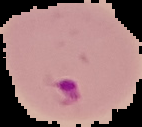
image_type: segmented cell region on a black background
image_size: 142×127 pixels
preparation: thin blood smear
result: Plasmodium parasites identified